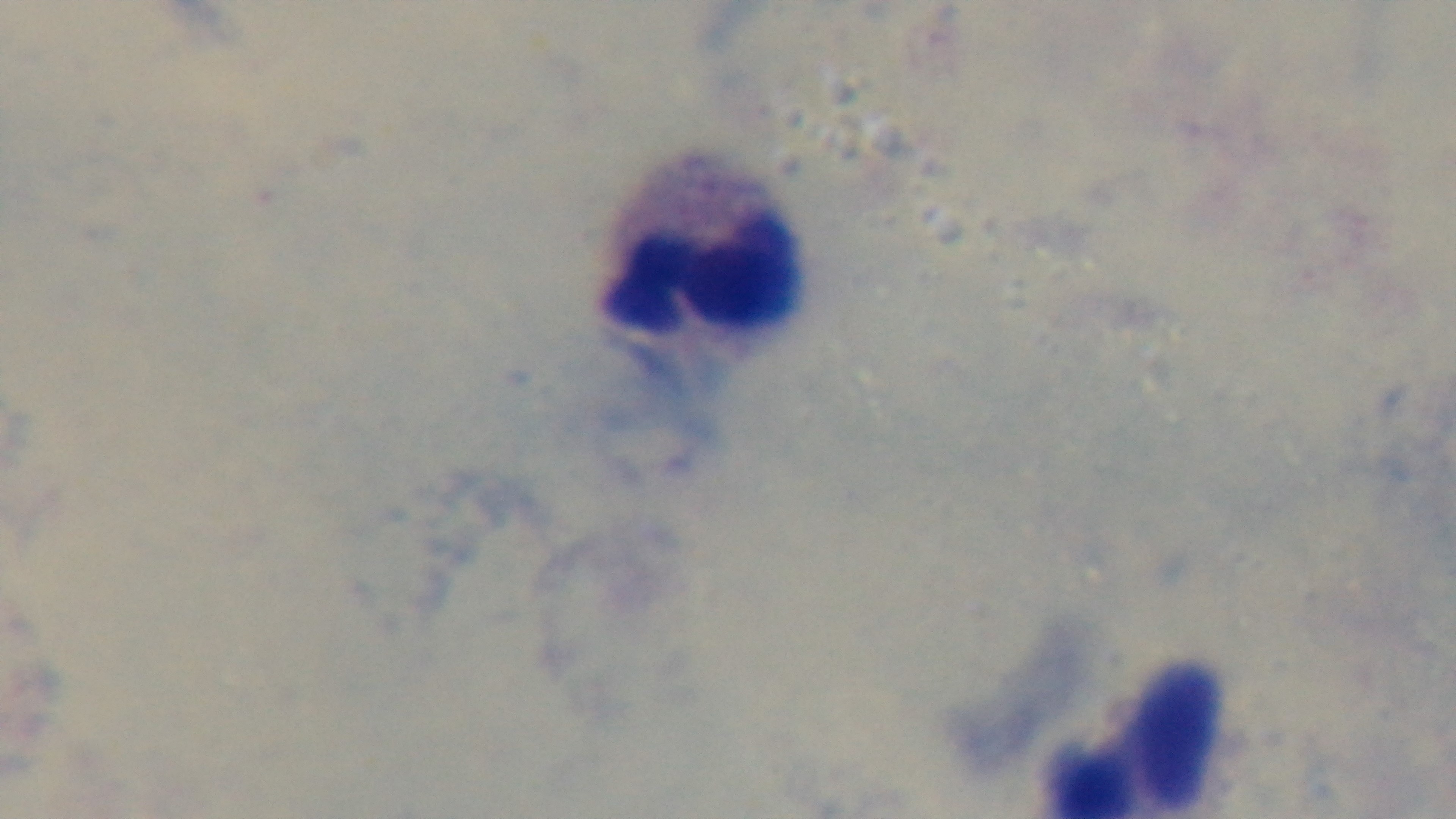
Summary:
  - Capture: mounted 4K digital camera
  - Malaria status: uninfected
  - Preparation: thick
  - Field of view: single
  - Stain: Giemsa
  - Objective: 100x oil immersion
  - Modality: light microscopy